Classify this cell by malaria status.
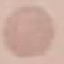
Uninfected.

Cell patch, automatically extracted from a larger field of view and resized to 64 × 64 pixels. Giemsa-stained preparation. Thin smear of blood. Photographed with a smartphone camera at the microscope eyepiece.